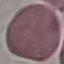

Summary:
  - Result: no malaria parasites detected
  - Stain: Giemsa
  - Preparation: thin blood film
  - Image type: cell patch, automatically extracted from a larger field of view and resized to 64 × 64 pixels
  - Capture: smartphone through the microscope eyepiece